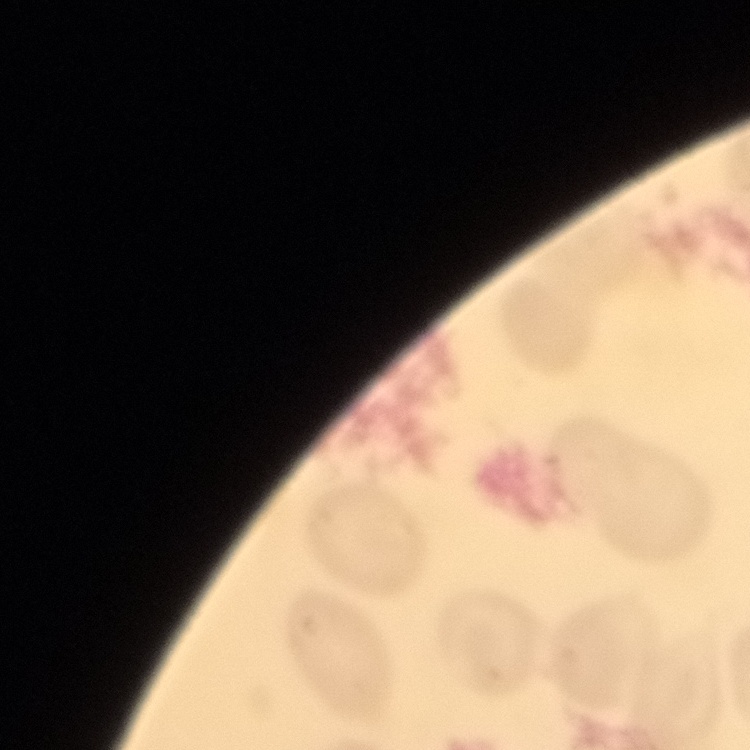 The red blood cells exhibit no rouleaux formation. Thin blood film. Stained with either Field's or Giemsa. Square crop of a larger photomicrograph.